Assess the morphology of the red blood cells.
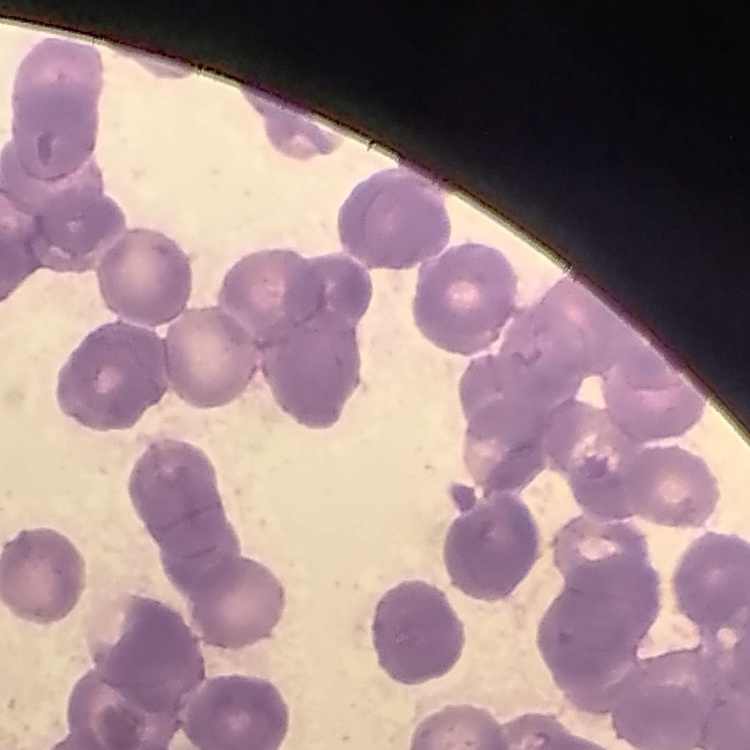

They show rouleaux formation.

Summary:
  - Preparation: thin peripheral smear
  - Image type: one tile cut from a larger photomicrograph
  - Stain: Field's or Giemsa